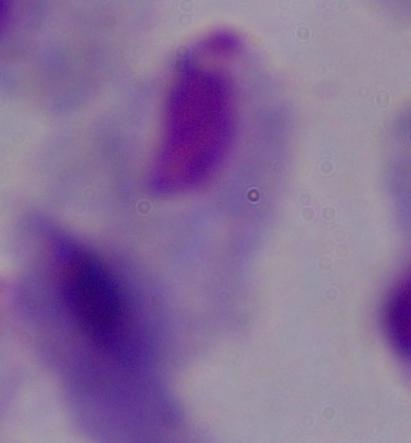

{
  "identification": "trichomonad",
  "modality": "photomicrograph",
  "magnification": "1000x"
}